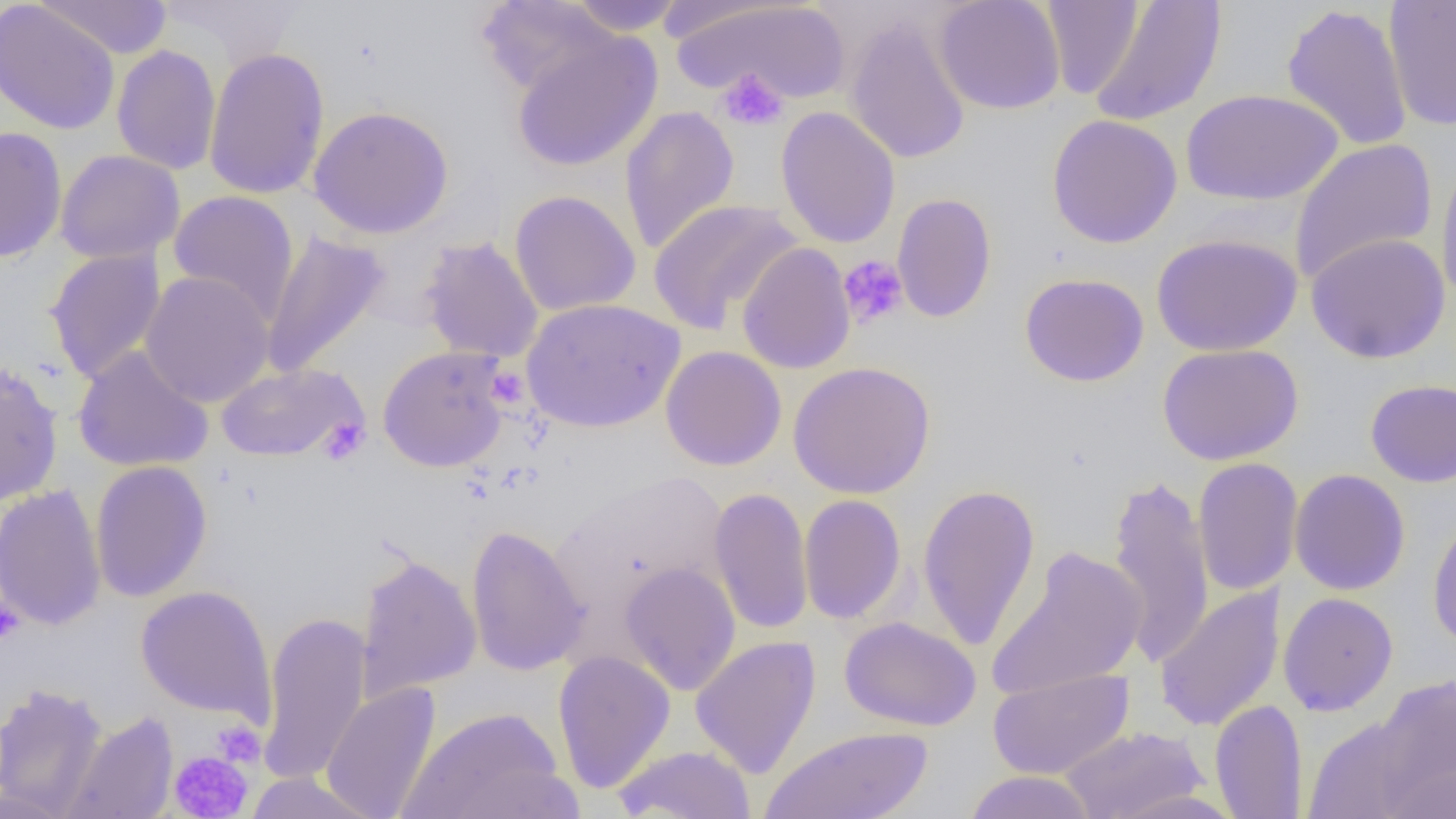
Summary:
  - Coordinate format: approximate bounding boxes as [x1, y1, x2, y2] in pixels
  - Uninfected red blood cell locations: [35, 0, 172, 60], [158, 0, 307, 69], [476, 0, 620, 98], [563, 0, 689, 35], [933, 0, 1066, 115], [1383, 0, 1456, 132], [0, 1, 120, 136], [670, 1, 851, 105], [1089, 1, 1227, 128], [1040, 2, 1142, 99], [1281, 3, 1414, 152], [844, 14, 973, 165], [511, 30, 663, 172], [111, 45, 222, 175], [203, 47, 331, 200], [1181, 88, 1343, 207], [308, 104, 454, 239], [619, 106, 740, 255], [775, 106, 901, 249], [1046, 114, 1183, 249], [0, 125, 67, 264], [1289, 139, 1438, 285], [55, 149, 185, 264], [1435, 157, 1456, 311], [168, 190, 299, 324], [509, 190, 641, 316], [892, 192, 997, 323], [647, 198, 803, 335], [261, 230, 391, 378], [1150, 232, 1303, 357], [1306, 232, 1450, 364], [419, 236, 544, 364], [736, 242, 856, 374], [45, 247, 166, 384], [140, 271, 275, 408], [1020, 272, 1149, 387], [521, 297, 686, 433], [1157, 343, 1304, 465], [73, 345, 214, 473], [660, 345, 787, 471], [377, 346, 511, 472], [0, 359, 63, 506], [788, 361, 936, 499], [215, 363, 367, 462], [1365, 378, 1456, 487], [1192, 457, 1303, 596], [89, 460, 212, 602], [1289, 469, 1411, 596], [1106, 471, 1214, 669], [0, 484, 107, 631], [918, 484, 1041, 651], [708, 487, 814, 635], [798, 494, 907, 625], [1427, 512, 1456, 652], [466, 524, 589, 676], [986, 546, 1147, 701], [355, 550, 482, 702], [619, 562, 741, 695], [135, 585, 276, 723], [1154, 585, 1286, 732], [1278, 592, 1398, 716], [257, 610, 373, 785], [838, 616, 981, 732], [690, 635, 821, 779], [552, 649, 676, 792], [988, 668, 1134, 779], [1372, 674, 1456, 809], [0, 682, 108, 817], [321, 682, 441, 819], [1209, 699, 1308, 819], [401, 706, 568, 819], [64, 711, 179, 819], [1301, 715, 1429, 819], [761, 726, 934, 819], [1059, 726, 1209, 819], [613, 744, 756, 819], [1382, 759, 1456, 819], [962, 770, 1097, 819], [242, 772, 384, 818], [1107, 789, 1245, 819]
  - Platelet locations: [716, 68, 789, 132], [837, 255, 909, 330], [495, 373, 525, 403], [317, 418, 370, 464], [0, 598, 24, 646], [211, 722, 265, 767], [168, 750, 253, 817]
  - Slide-level diagnosis: negative for blood parasites
  - Modality: light microscopy
  - Preparation: thin blood film
  - Image size: 1456×819 pixels
  - Magnification: 1000x
  - Field of view: single